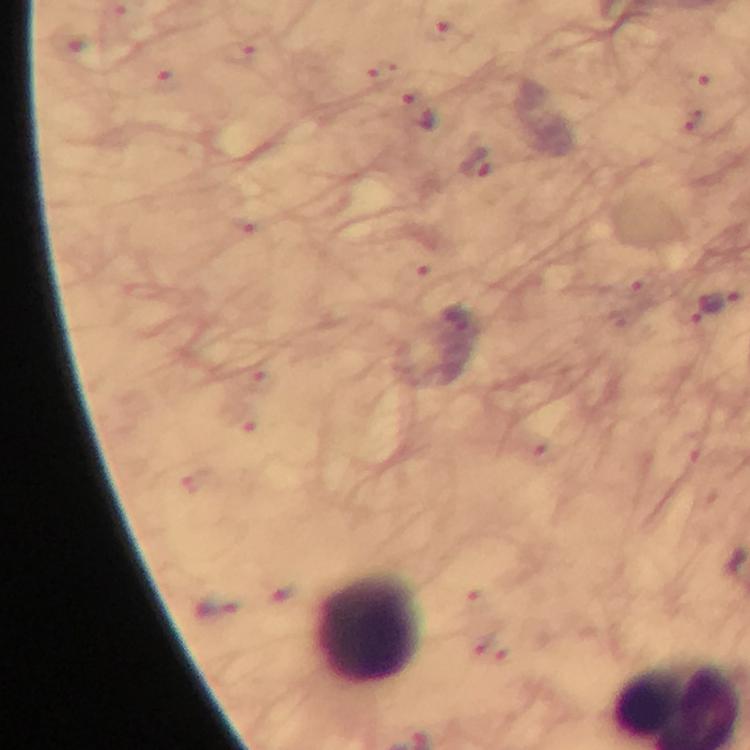
Approximate centers as (x, y) in pixels.
Summary:
  - Plasmodium parasite locations: (697, 79), (418, 110), (475, 162), (719, 303), (285, 592), (216, 611)
  - Leukocyte locations: (368, 631)
  - Capture: smartphone camera through the microscope
  - Image size: 750×750 pixels
  - Cropped from: a single field of view
  - Context: from a diagnostic examination for malaria
  - Immersion oil: used
  - Magnification: 100x
  - Stain: Giemsa
  - Preparation: thick smear